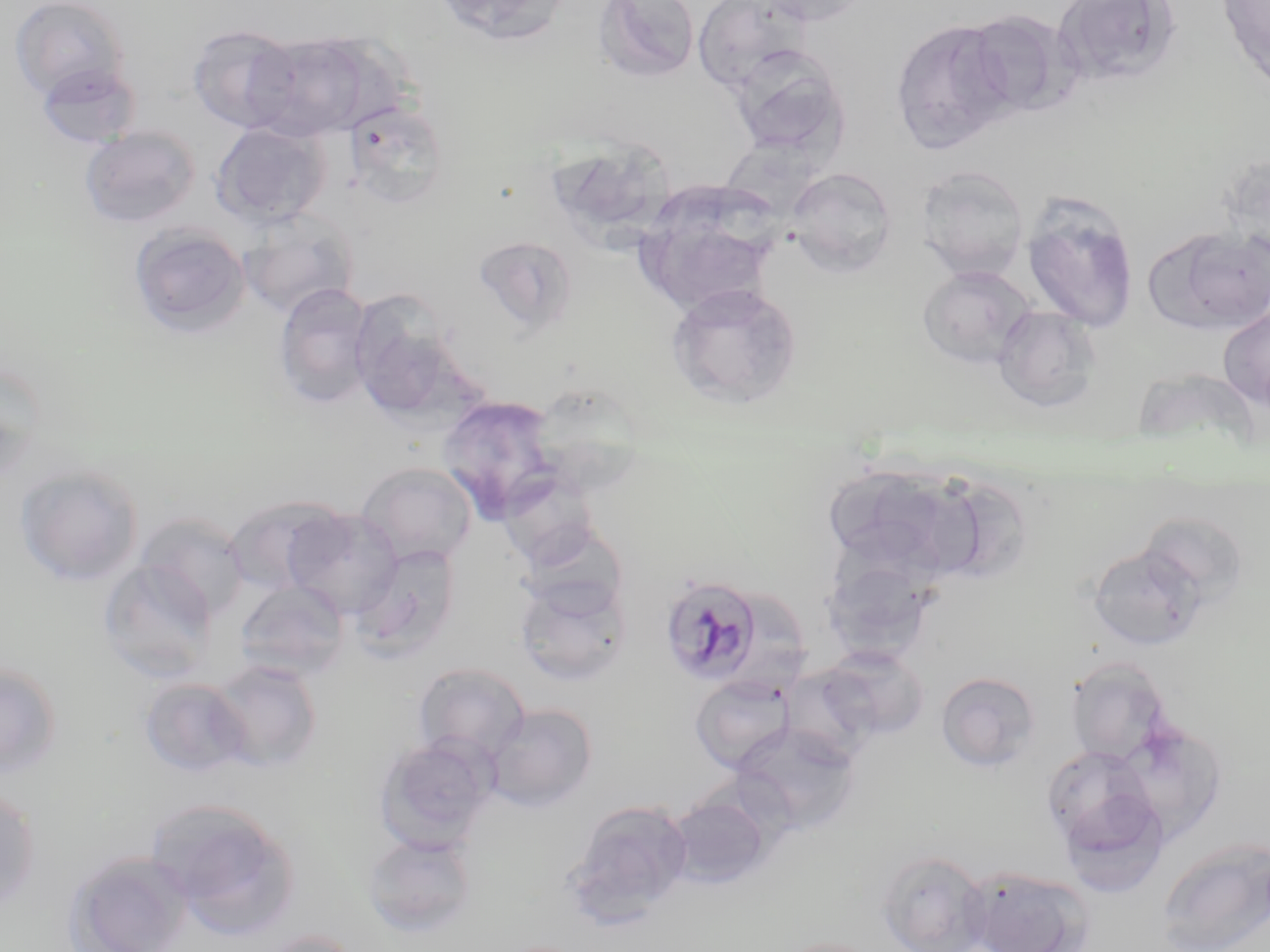 Approximate bounding boxes as (x1,y1)-(x2,y2) corner pairs in pixels. Uninfected red blood cell locations: (10,0)-(130,101), (430,0)-(571,46), (593,0)-(701,83), (692,0)-(813,92), (749,0)-(877,26), (1052,0)-(1184,86), (1217,0)-(1270,92), (960,10)-(1080,118), (891,19)-(1017,153), (186,24)-(300,133), (247,32)-(378,140), (728,46)-(850,161), (36,63)-(141,149), (343,99)-(451,210), (211,121)-(332,229), (79,125)-(201,229), (546,139)-(677,248), (1219,153)-(1269,258), (916,164)-(1030,280), (786,167)-(897,276), (633,190)-(783,314), (1021,193)-(1140,333), (238,211)-(358,319), (129,222)-(252,338), (1143,226)-(1270,334), (472,235)-(579,337), (918,265)-(1037,369), (666,281)-(803,409), (273,282)-(378,409), (992,305)-(1103,412), (1218,307)-(1270,410), (351,313)-(474,422), (0,360)-(45,487), (436,395)-(565,520), (356,462)-(478,567), (823,462)-(986,587), (13,463)-(145,587), (496,468)-(603,568), (225,495)-(345,597), (282,506)-(403,619), (135,512)-(251,621), (352,543)-(462,661), (1087,543)-(1206,653), (818,546)-(942,662), (98,558)-(218,684), (513,574)-(632,686), (235,580)-(349,680), (818,645)-(930,742), (1065,657)-(1174,765), (207,659)-(324,773), (0,662)-(63,779), (413,663)-(531,764), (779,663)-(882,766), (936,671)-(1041,773), (690,673)-(797,774), (138,677)-(251,778), (695,677)-(875,802), (484,704)-(597,812), (733,721)-(862,835), (374,735)-(497,853), (1041,743)-(1165,868), (0,786)-(41,913), (667,794)-(771,889), (146,796)-(299,934), (565,799)-(694,923), (362,832)-(478,937), (1157,839)-(1270,951), (63,850)-(195,952), (876,850)-(992,952), (962,866)-(1095,952), (253,929)-(365,952), (769,936)-(887,952). Plasmodium malariae-infected red blood cell locations: (659,574)-(763,685). Slide-level diagnosis: Plasmodium malariae. Optical microscopy. Single field of view. May-Grünwald-Giemsa stain. Image is 1270×952 pixels. 1000x magnification. Thin blood smear.